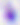

Summary:
  - Identification: Toxoplasma gondii
  - Modality: micrograph
  - Magnification: 400x